Report the malaria status of this cell.
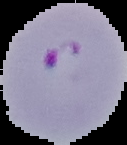

It is parasitized.

From a thin blood smear. The area outside the segmented cell region is set to black. Image is 127×145 pixels.